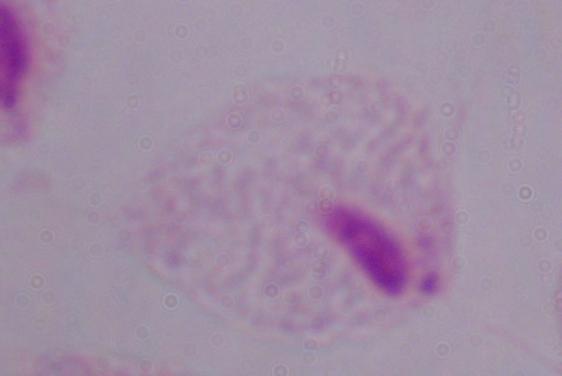

A trichomonad is shown. Photomicrograph. 1000x magnification.